Comment on the morphology of the red blood cells.
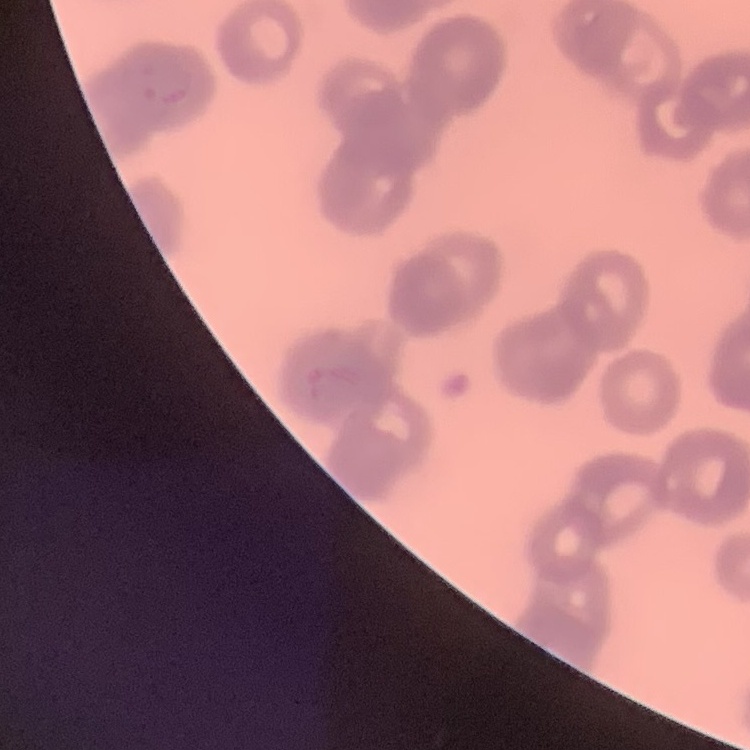
They show rouleaux formation.

Stained with either Field's or Giemsa. Thin blood film. One tile cut from a larger photomicrograph.